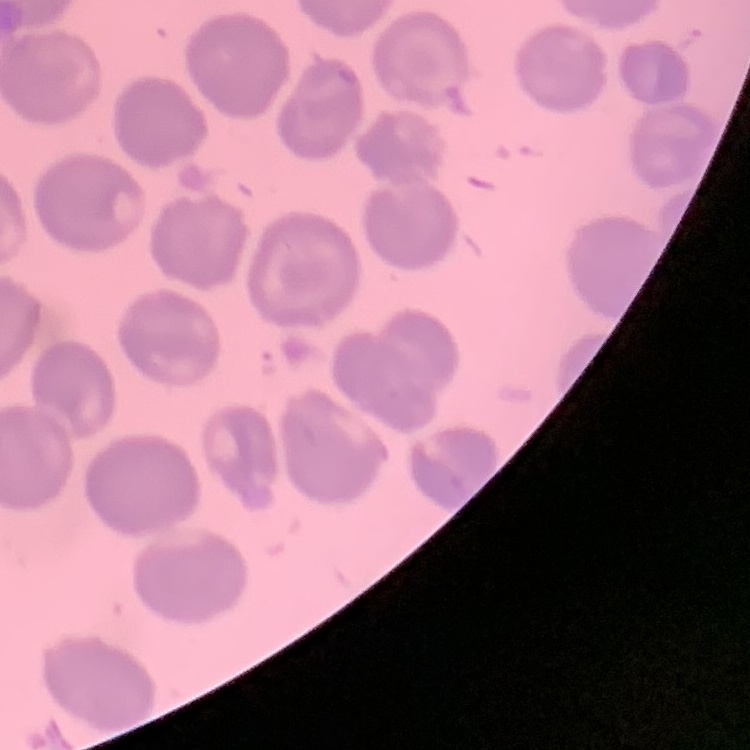
The erythrocytes exhibit no rouleaux formation. Thin blood film. Stained with either Field's or Giemsa. Square crop of a larger photomicrograph.